Outline each blood parasite and name the species.
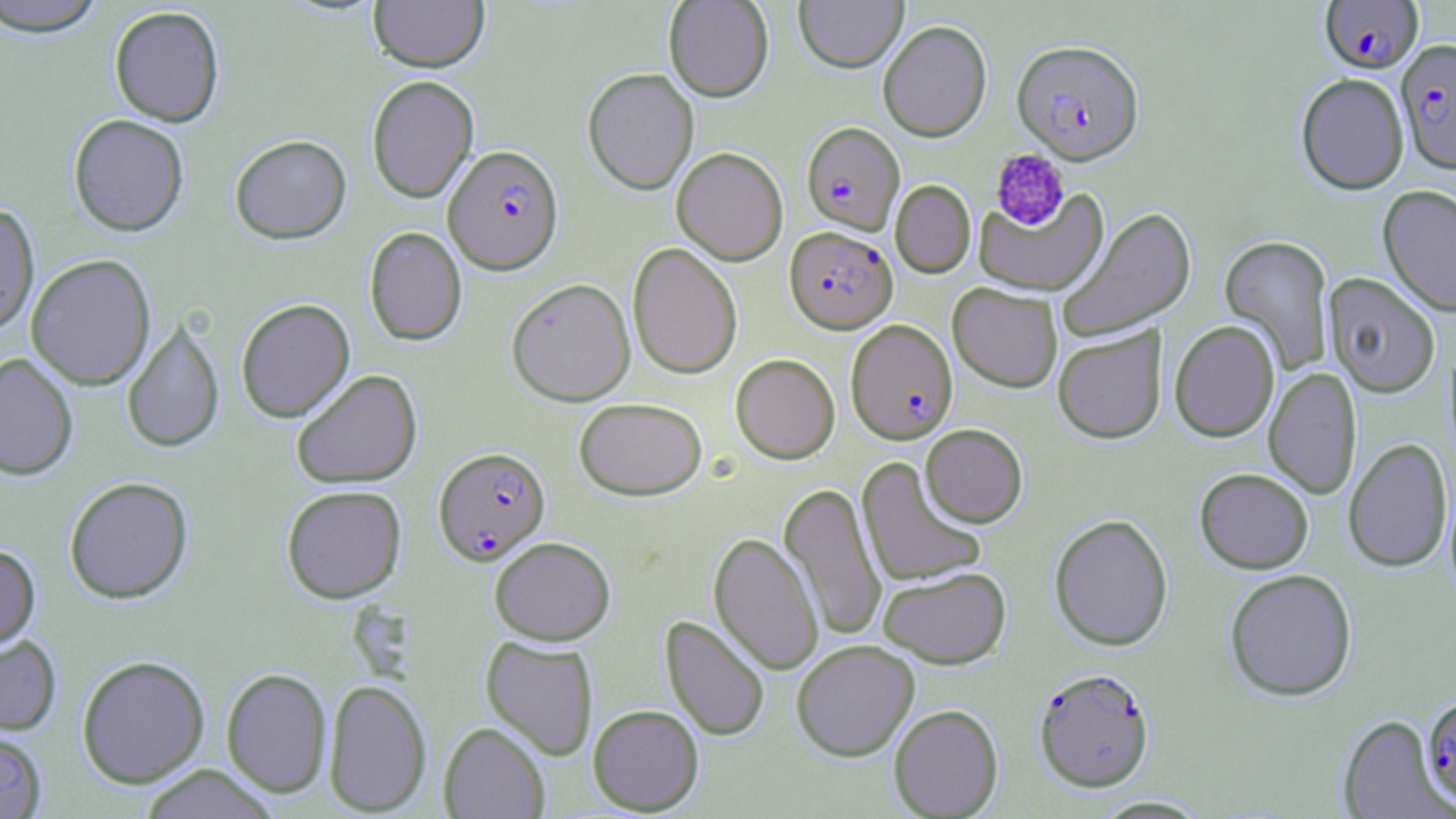
Approximate bounding boxes as named x1/y1/x2/y2 corners in pixels.
Plasmodium falciparum-infected red blood cells: (x1=1319, y1=1, x2=1423, y2=76), (x1=1396, y1=40, x2=1456, y2=175), (x1=1012, y1=41, x2=1144, y2=165), (x1=802, y1=122, x2=905, y2=235), (x1=444, y1=144, x2=564, y2=274), (x1=784, y1=226, x2=897, y2=333), (x1=846, y1=319, x2=958, y2=445), (x1=433, y1=446, x2=550, y2=564), (x1=1033, y1=667, x2=1154, y2=792), (x1=1421, y1=695, x2=1456, y2=808).
No Plasmodium ovale, Plasmodium malariae, Plasmodium vivax, Babesia divergens, or Trypanosoma brucei observed.

Summary:
  - Platelet locations: (x1=990, y1=149, x2=1070, y2=230)
  - Uninfected red blood cell locations: (x1=0, y1=0, x2=108, y2=38), (x1=369, y1=0, x2=490, y2=73), (x1=663, y1=0, x2=774, y2=102), (x1=794, y1=0, x2=908, y2=73), (x1=109, y1=6, x2=225, y2=127), (x1=878, y1=20, x2=992, y2=142), (x1=583, y1=67, x2=699, y2=195), (x1=1295, y1=73, x2=1409, y2=195), (x1=366, y1=75, x2=479, y2=204), (x1=68, y1=114, x2=189, y2=236), (x1=229, y1=134, x2=351, y2=244), (x1=672, y1=147, x2=788, y2=265), (x1=891, y1=180, x2=975, y2=278), (x1=1378, y1=185, x2=1456, y2=318), (x1=974, y1=189, x2=1109, y2=297), (x1=0, y1=202, x2=40, y2=335), (x1=1056, y1=206, x2=1196, y2=343), (x1=364, y1=226, x2=467, y2=346), (x1=1220, y1=234, x2=1335, y2=374), (x1=627, y1=242, x2=743, y2=379), (x1=26, y1=254, x2=156, y2=391), (x1=1323, y1=273, x2=1440, y2=398), (x1=506, y1=277, x2=636, y2=406), (x1=948, y1=282, x2=1063, y2=393), (x1=236, y1=298, x2=355, y2=423), (x1=122, y1=318, x2=225, y2=454), (x1=1169, y1=320, x2=1280, y2=442), (x1=1053, y1=326, x2=1167, y2=444), (x1=0, y1=352, x2=78, y2=480), (x1=730, y1=353, x2=840, y2=464), (x1=1264, y1=367, x2=1362, y2=500), (x1=290, y1=369, x2=423, y2=489), (x1=574, y1=397, x2=707, y2=500), (x1=921, y1=423, x2=1028, y2=527), (x1=1344, y1=438, x2=1453, y2=573), (x1=856, y1=457, x2=988, y2=588), (x1=1194, y1=468, x2=1314, y2=574), (x1=64, y1=476, x2=194, y2=604), (x1=779, y1=482, x2=887, y2=642), (x1=281, y1=485, x2=407, y2=603), (x1=1049, y1=513, x2=1173, y2=651), (x1=709, y1=532, x2=823, y2=676), (x1=489, y1=536, x2=615, y2=645), (x1=0, y1=543, x2=40, y2=651), (x1=878, y1=566, x2=1011, y2=669), (x1=1224, y1=569, x2=1358, y2=701), (x1=661, y1=615, x2=771, y2=742), (x1=0, y1=633, x2=62, y2=736), (x1=481, y1=636, x2=599, y2=760), (x1=791, y1=639, x2=919, y2=761), (x1=76, y1=655, x2=210, y2=788), (x1=221, y1=667, x2=332, y2=797), (x1=323, y1=678, x2=432, y2=815), (x1=588, y1=704, x2=704, y2=815), (x1=888, y1=704, x2=1003, y2=818), (x1=1338, y1=715, x2=1452, y2=818), (x1=439, y1=722, x2=550, y2=818), (x1=0, y1=729, x2=48, y2=818), (x1=138, y1=765, x2=280, y2=819), (x1=1090, y1=795, x2=1213, y2=818)
  - Slide-level diagnosis: Plasmodium falciparum
  - Modality: optical microscopy
  - Field of view: single
  - Stain: May-Grünwald-Giemsa
  - Preparation: thin blood smear
  - Image size: 1456×819 pixels
  - Magnification: 1000x